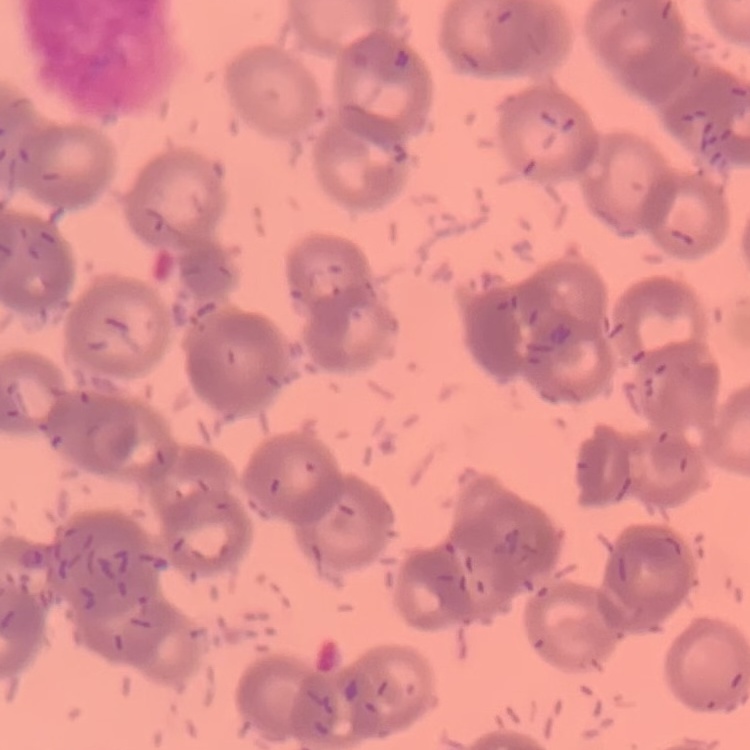 The red blood cells exhibit rouleaux formation. Stained with either Field's or Giemsa. One tile cut from a larger photomicrograph. Thin blood film.